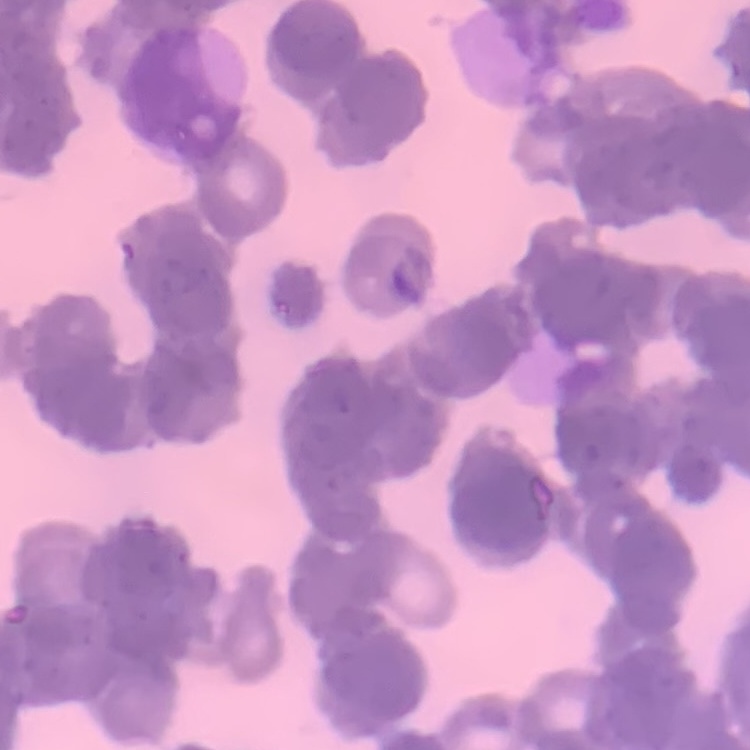
Summary:
  - Erythrocyte morphology: rouleaux formation
  - Preparation: thin blood film
  - Stain: Field's or Giemsa
  - Image type: one tile cut from a larger photomicrograph